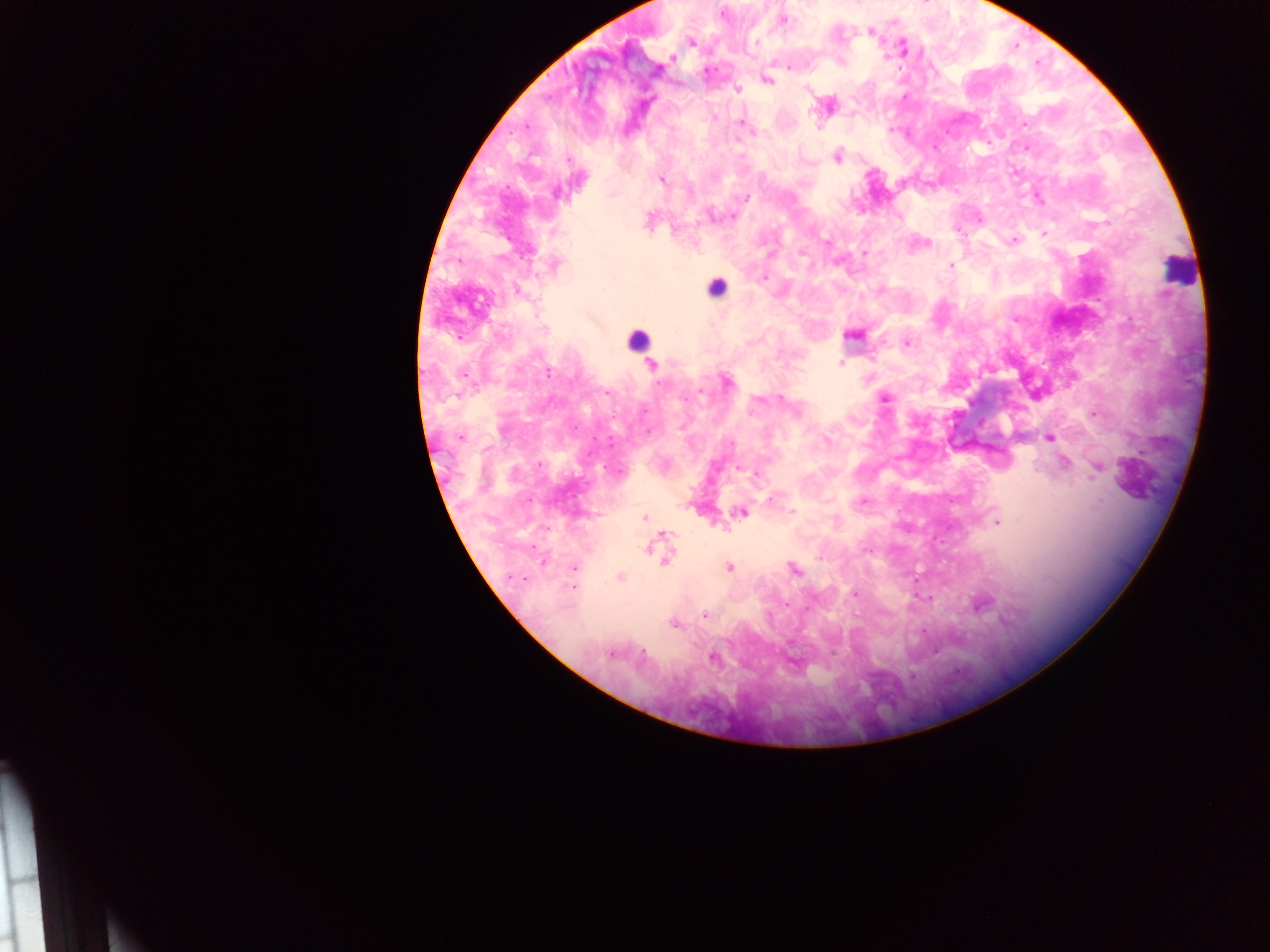
image size = 1270×952 pixels
Plasmodium parasite locations = approximate centers as {x, y} in pixels: {721, 13}, {782, 20}, {869, 31}, {691, 42}, {756, 42}, {902, 49}, {672, 57}, {789, 66}, {657, 69}, {766, 80}, {736, 89}, {826, 106}, {741, 122}, {1023, 123}, {837, 155}, {1013, 172}, {660, 179}, {746, 198}, {1037, 198}, {731, 216}, {648, 221}, {1043, 233}, {1013, 241}, {923, 243}, {863, 253}, {554, 265}, {950, 266}, {517, 289}, {1015, 319}, {852, 334}, {906, 342}, {841, 363}, {651, 365}, {726, 380}, {884, 398}, {1093, 414}, {461, 437}, {1049, 437}, {1064, 463}, {740, 467}, {1097, 467}, {616, 471}, {756, 473}, {771, 499}, {861, 502}, {742, 511}, {792, 512}, {645, 518}, {996, 521}, {662, 534}, {649, 546}, {664, 556}, {573, 566}, {728, 567}, {792, 568}, {621, 576}, {855, 593}, {929, 598}, {979, 603}, {704, 613}, {674, 623}, {611, 652}, {713, 656}
leukocyte locations = approximate centers as {x, y} in pixels: {1179, 269}, {715, 288}, {636, 340}
capture = mobile-phone photograph through a microscope
country = Ghana
field of view = single
preparation = thick blood smear